State which parasite is depicted.
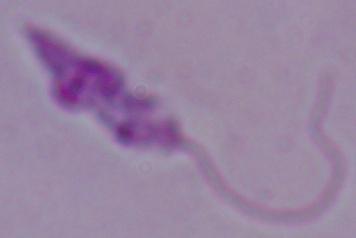
Leishmania.

Summary:
  - Modality: micrograph
  - Magnification: 1000x